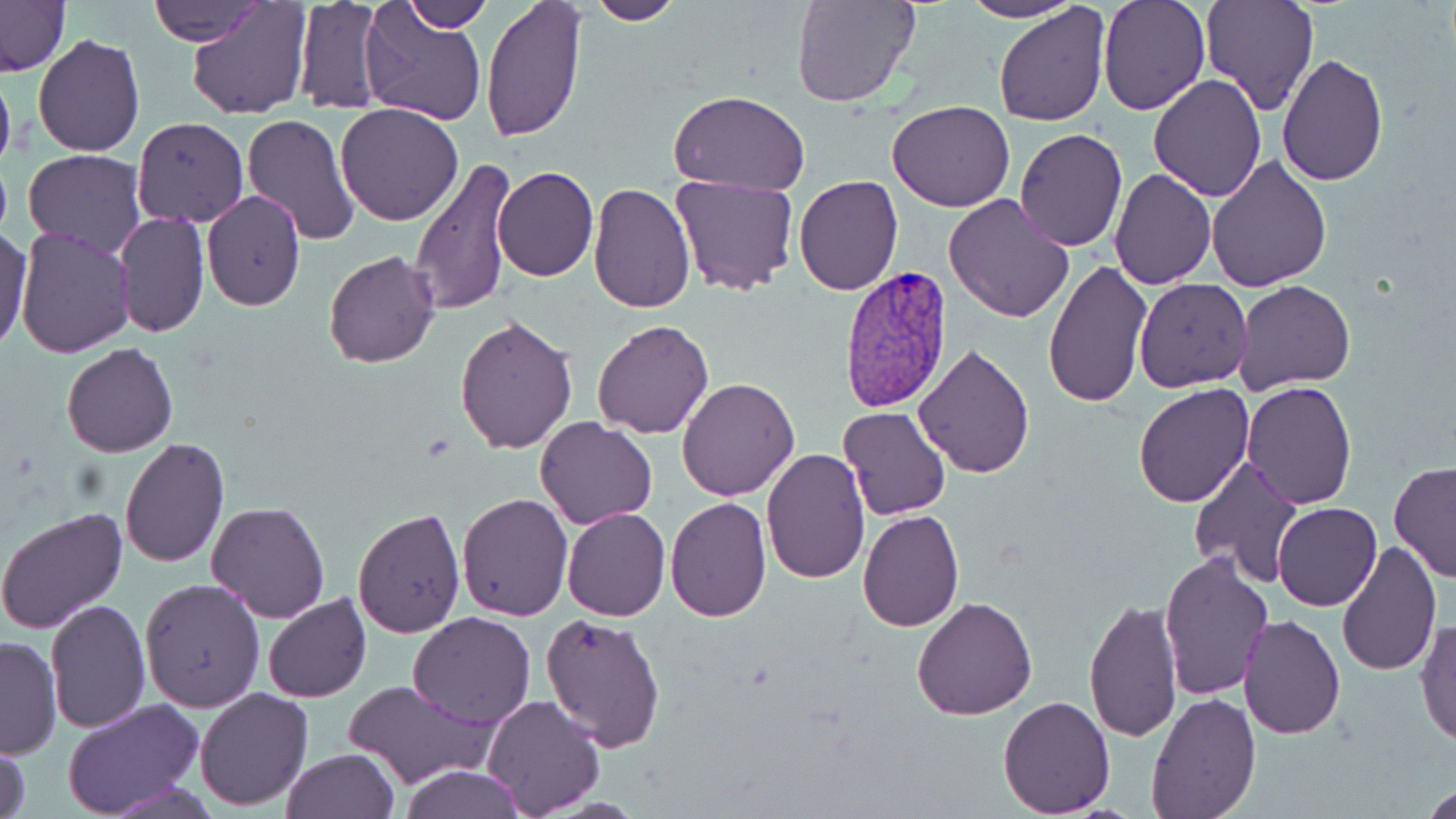

Approximate bounding boxes as [x1, y1, x2, y2] in pixels. Plasmodium vivax-infected red blood cell locations: [836, 263, 955, 415]. Uninfected red blood cell locations: [145, 0, 270, 46], [186, 0, 311, 119], [292, 0, 391, 118], [396, 0, 493, 32], [481, 0, 587, 142], [587, 0, 680, 25], [793, 0, 919, 108], [961, 0, 1083, 23], [1098, 0, 1209, 115], [1200, 0, 1319, 116], [1, 1, 71, 75], [992, 2, 1110, 126], [359, 5, 487, 127], [31, 33, 145, 158], [1278, 53, 1388, 186], [0, 62, 15, 180], [1149, 76, 1266, 202], [668, 90, 809, 196], [888, 99, 1015, 212], [335, 103, 464, 225], [241, 113, 360, 246], [131, 117, 249, 227], [1013, 129, 1128, 251], [22, 149, 145, 259], [1205, 154, 1331, 290], [409, 157, 517, 315], [491, 166, 598, 282], [1110, 169, 1217, 289], [669, 176, 799, 296], [793, 176, 903, 294], [588, 184, 697, 315], [201, 189, 305, 311], [943, 192, 1076, 322], [113, 210, 208, 339], [0, 225, 32, 351], [15, 227, 138, 359], [322, 249, 441, 369], [1042, 258, 1152, 409], [1134, 277, 1254, 392], [1234, 279, 1356, 393], [1135, 309, 1257, 473], [454, 314, 579, 455], [590, 319, 714, 439], [62, 342, 177, 457], [914, 344, 1034, 478], [676, 377, 800, 501], [1241, 381, 1357, 509], [1133, 383, 1255, 507], [837, 405, 952, 521], [537, 417, 656, 529], [118, 438, 231, 569], [761, 448, 870, 584], [1187, 454, 1304, 588], [1388, 459, 1456, 584], [457, 493, 573, 621], [665, 497, 772, 622], [206, 500, 329, 622], [1273, 502, 1382, 610], [0, 506, 128, 634], [352, 506, 465, 637], [561, 508, 669, 621], [856, 508, 965, 631], [1337, 538, 1442, 675], [1157, 550, 1271, 700], [140, 579, 263, 712], [263, 595, 372, 703], [912, 596, 1038, 720], [1084, 598, 1183, 743], [44, 599, 151, 735], [407, 612, 536, 729], [540, 612, 668, 753], [1237, 614, 1345, 740], [1415, 617, 1456, 747], [0, 634, 61, 759], [343, 679, 493, 788], [192, 687, 312, 810], [1145, 692, 1261, 818], [480, 693, 606, 816], [998, 695, 1115, 817], [62, 699, 204, 819], [0, 740, 32, 819], [282, 747, 399, 819], [397, 764, 526, 819], [1421, 784, 1456, 818]. Slide-level diagnosis: Plasmodium vivax. Captured at 1000x magnification. Thin blood smear. May-Grünwald-Giemsa-stained preparation. Optical microscopy. One field of a larger specimen. Image is 1456×819 pixels.